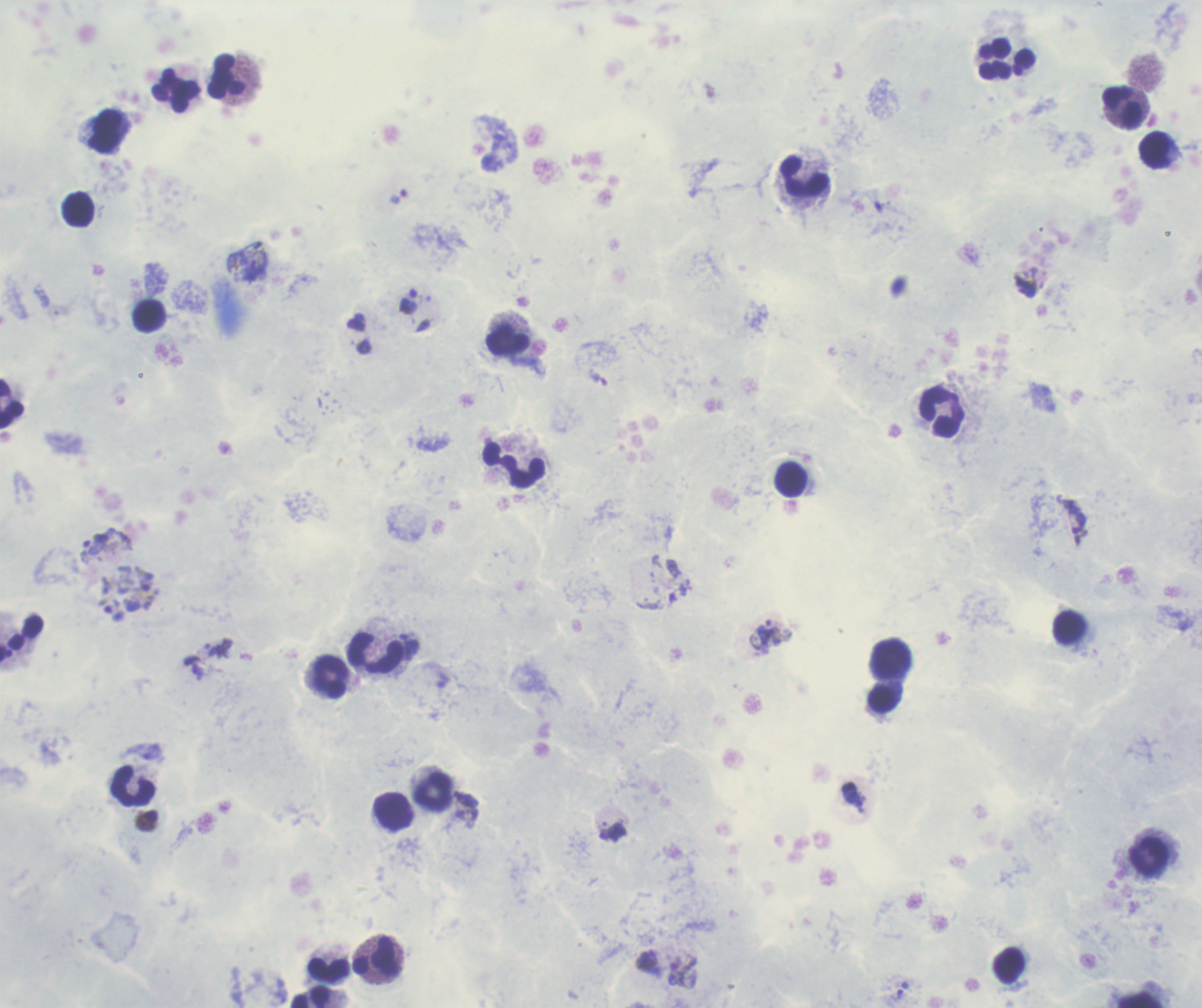

coordinate format = approximate centers as [x, y] in pixels
gametocyte locations = [683, 971]
leukocyte locations = [1006, 60], [228, 77], [177, 92], [1122, 108], [105, 129], [1157, 151], [804, 178], [78, 210], [509, 342], [11, 406], [942, 414], [515, 464], [791, 480], [375, 652], [890, 659], [331, 678], [882, 697], [133, 787], [434, 793], [394, 812], [1149, 856], [376, 956], [329, 970], [311, 996], [1142, 999]
trophozoite locations = [398, 196], [408, 301], [108, 543], [766, 635], [900, 991]
life-cycle stages observed = trophozoite, gametocyte
result = positive for Plasmodium parasites
image size = 1202×1008 pixels
background quality = unsatisfactory
field of view = one from this slide
magnification = 100x
stain = Romanowsky
context = previously used in a real diagnosis
coloration quality = good
preparation = thick blood smear